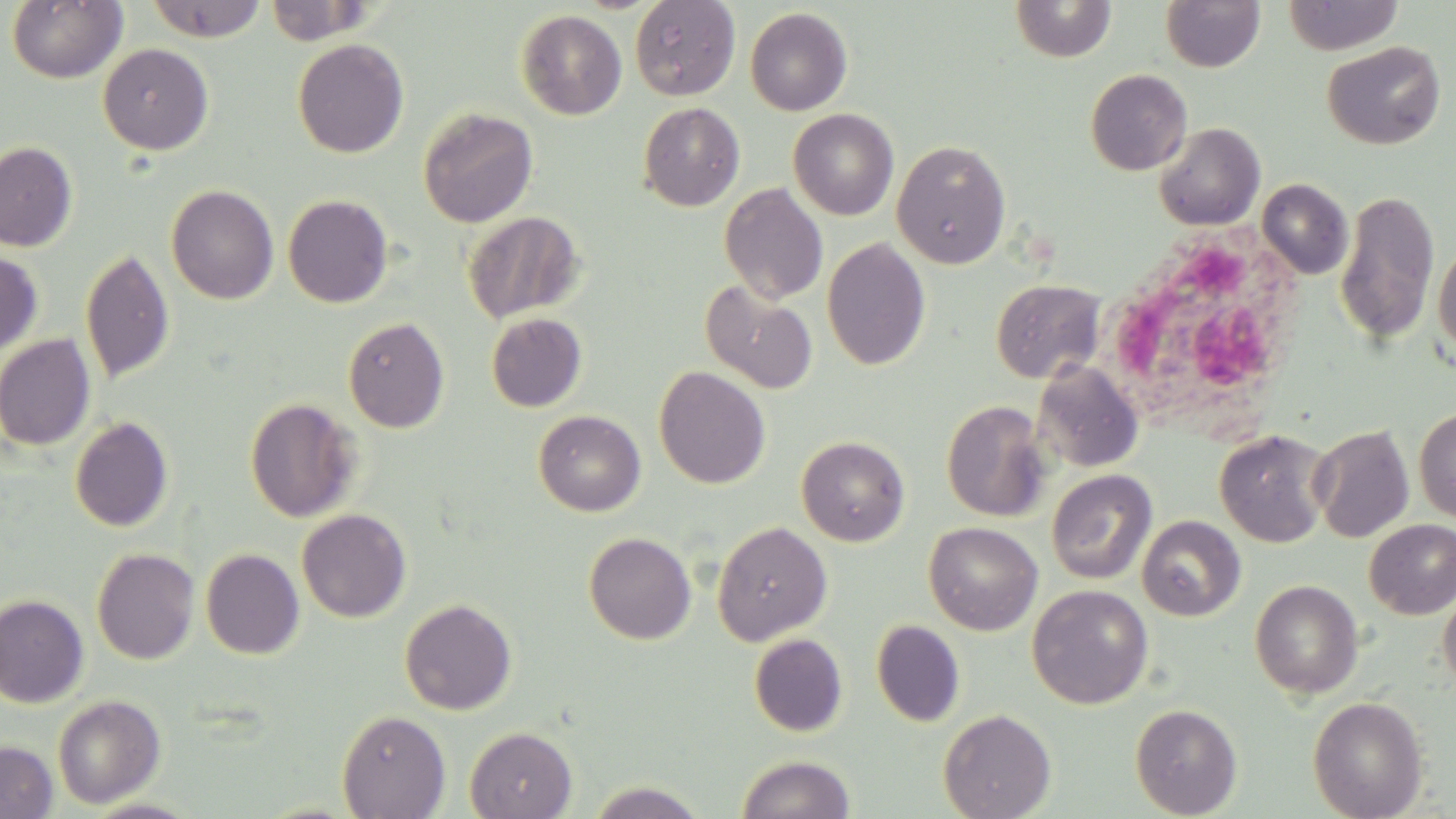

slide-level diagnosis = no evidence of blood parasites
uninfected red blood cell locations = approximate bounding boxes as (x1, y1, x2, y2) in pixels: (6, 0, 127, 84), (145, 0, 268, 42), (630, 0, 740, 100), (1010, 0, 1116, 62), (1160, 0, 1265, 72), (1282, 0, 1404, 55), (265, 1, 375, 45), (745, 7, 852, 115), (516, 10, 627, 120), (292, 38, 409, 158), (1322, 41, 1446, 150), (98, 43, 213, 155), (1085, 69, 1192, 175), (638, 102, 745, 211), (418, 107, 538, 228), (788, 108, 899, 220), (1153, 122, 1265, 231), (892, 139, 1012, 269), (0, 142, 77, 251), (1257, 178, 1353, 279), (719, 183, 828, 304), (166, 184, 279, 304), (1335, 188, 1440, 347), (282, 194, 394, 307), (462, 211, 584, 323), (821, 237, 931, 370), (1433, 241, 1456, 359), (0, 248, 43, 355), (80, 248, 175, 384), (990, 279, 1105, 383), (700, 280, 818, 395), (486, 312, 587, 412), (343, 316, 450, 432), (0, 334, 96, 450), (1032, 360, 1144, 473), (654, 365, 771, 488), (245, 397, 362, 522), (940, 399, 1052, 521), (1414, 408, 1456, 522), (533, 410, 646, 516), (69, 416, 174, 532), (1310, 424, 1415, 543), (1214, 429, 1332, 548), (796, 435, 909, 546), (1046, 470, 1157, 585), (296, 508, 412, 623), (1137, 516, 1246, 621), (1364, 519, 1456, 619), (712, 520, 832, 646), (924, 521, 1043, 635), (584, 531, 696, 644), (91, 548, 200, 664), (200, 548, 304, 659), (1249, 579, 1364, 699), (1027, 584, 1153, 709), (1438, 586, 1456, 693), (0, 594, 89, 708), (399, 597, 517, 715), (871, 619, 965, 727), (748, 633, 848, 736), (52, 694, 165, 808), (1307, 696, 1428, 818), (1130, 702, 1242, 818), (938, 708, 1056, 819), (336, 710, 450, 818), (464, 726, 577, 819), (0, 740, 58, 819), (736, 754, 855, 819), (584, 781, 709, 818)
modality = optical microscopy
image size = 1456×819 pixels
preparation = thin blood film
stain = May-Grünwald-Giemsa
field of view = one of a larger specimen
magnification = 1000x
white blood cell locations = approximate bounding boxes as (x1, y1, x2, y2) in pixels: (1089, 229, 1312, 438)